Outline each uninfected red blood cell.
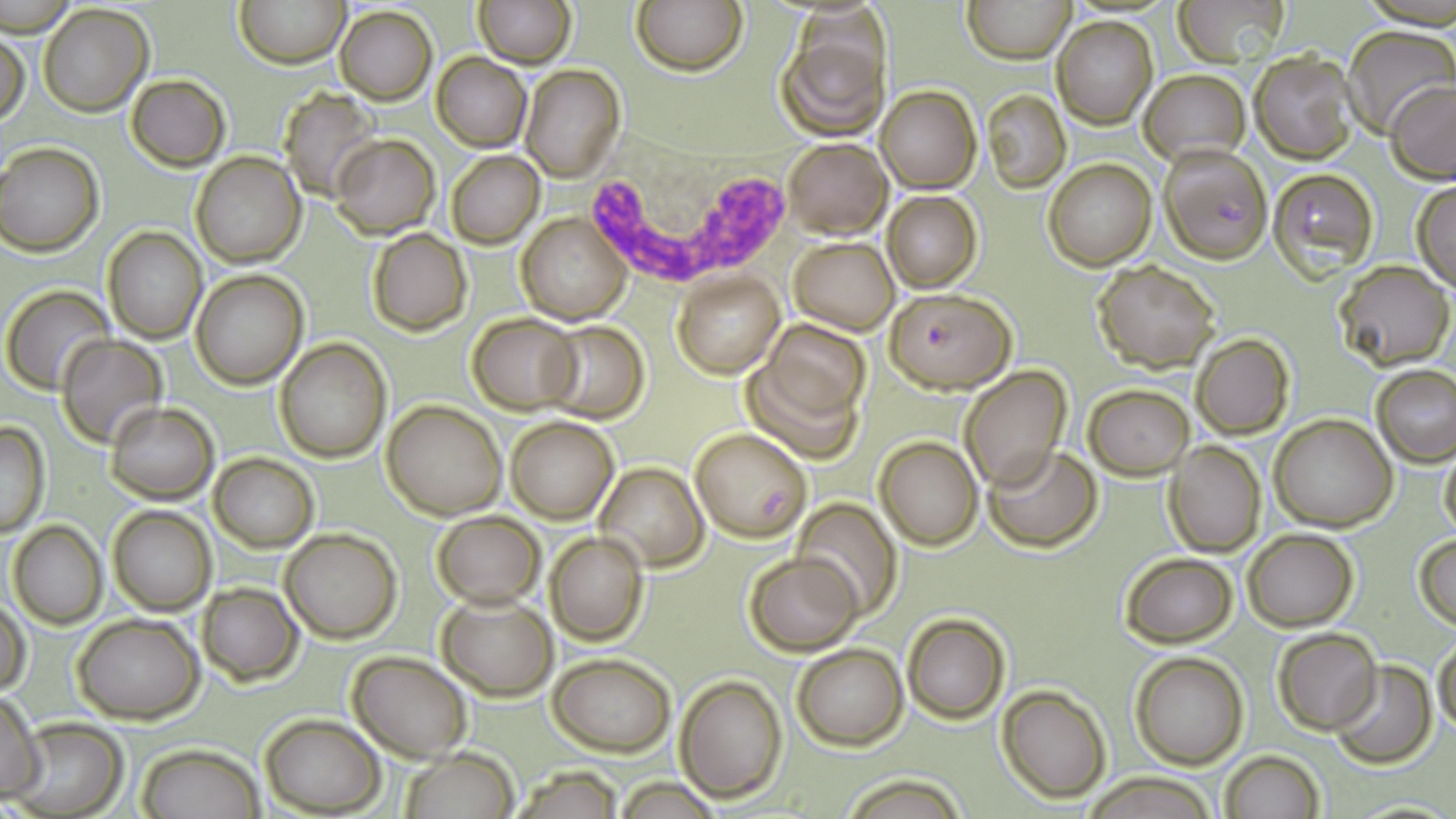
Approximate bounding boxes as named x1/y1/x2/y2 corners in pixels.
Uninfected red blood cells: (x1=236, y1=0, x2=348, y2=68), (x1=474, y1=0, x2=574, y2=68), (x1=633, y1=0, x2=745, y2=75), (x1=964, y1=0, x2=1073, y2=62), (x1=1175, y1=0, x2=1289, y2=66), (x1=39, y1=4, x2=154, y2=115), (x1=335, y1=6, x2=437, y2=104), (x1=1052, y1=16, x2=1157, y2=127), (x1=774, y1=19, x2=889, y2=143), (x1=1343, y1=26, x2=1454, y2=137), (x1=1, y1=28, x2=30, y2=129), (x1=1249, y1=50, x2=1359, y2=164), (x1=431, y1=53, x2=531, y2=151), (x1=519, y1=65, x2=626, y2=182), (x1=1138, y1=70, x2=1249, y2=167), (x1=127, y1=74, x2=230, y2=171), (x1=1385, y1=78, x2=1456, y2=183), (x1=876, y1=85, x2=981, y2=192), (x1=282, y1=86, x2=380, y2=200), (x1=984, y1=91, x2=1069, y2=191), (x1=332, y1=134, x2=439, y2=239), (x1=781, y1=138, x2=892, y2=238), (x1=0, y1=142, x2=104, y2=255), (x1=446, y1=149, x2=545, y2=248), (x1=190, y1=151, x2=306, y2=267), (x1=1044, y1=160, x2=1155, y2=270), (x1=1410, y1=182, x2=1456, y2=290), (x1=882, y1=191, x2=982, y2=293), (x1=517, y1=213, x2=630, y2=325), (x1=102, y1=228, x2=206, y2=344), (x1=367, y1=229, x2=471, y2=337), (x1=789, y1=237, x2=899, y2=334), (x1=1091, y1=259, x2=1221, y2=371), (x1=1331, y1=261, x2=1453, y2=369), (x1=190, y1=271, x2=307, y2=389), (x1=672, y1=272, x2=784, y2=379), (x1=2, y1=285, x2=114, y2=394), (x1=468, y1=313, x2=582, y2=414), (x1=539, y1=321, x2=649, y2=422), (x1=764, y1=322, x2=869, y2=422), (x1=1191, y1=333, x2=1294, y2=440), (x1=54, y1=334, x2=168, y2=446), (x1=275, y1=338, x2=390, y2=462), (x1=742, y1=355, x2=863, y2=466), (x1=1372, y1=365, x2=1456, y2=467), (x1=958, y1=366, x2=1070, y2=493), (x1=1082, y1=384, x2=1194, y2=479), (x1=381, y1=400, x2=507, y2=519), (x1=103, y1=401, x2=219, y2=503), (x1=1270, y1=414, x2=1397, y2=531), (x1=506, y1=416, x2=617, y2=524), (x1=0, y1=420, x2=50, y2=537), (x1=874, y1=436, x2=982, y2=550), (x1=1164, y1=441, x2=1265, y2=555), (x1=984, y1=444, x2=1102, y2=551), (x1=1438, y1=446, x2=1456, y2=541), (x1=208, y1=453, x2=318, y2=552), (x1=595, y1=462, x2=708, y2=571), (x1=791, y1=500, x2=904, y2=620), (x1=106, y1=504, x2=216, y2=616), (x1=431, y1=511, x2=544, y2=609), (x1=7, y1=521, x2=106, y2=628), (x1=281, y1=528, x2=401, y2=642), (x1=1242, y1=529, x2=1358, y2=631), (x1=545, y1=531, x2=648, y2=645), (x1=1413, y1=534, x2=1456, y2=629), (x1=1118, y1=551, x2=1238, y2=647), (x1=743, y1=552, x2=862, y2=656), (x1=196, y1=582, x2=304, y2=686), (x1=435, y1=591, x2=559, y2=701), (x1=1, y1=598, x2=31, y2=699), (x1=902, y1=613, x2=1009, y2=725), (x1=72, y1=614, x2=203, y2=723), (x1=1272, y1=628, x2=1382, y2=734), (x1=1433, y1=640, x2=1456, y2=736), (x1=790, y1=643, x2=907, y2=750), (x1=347, y1=650, x2=473, y2=762), (x1=1129, y1=650, x2=1250, y2=769), (x1=547, y1=651, x2=676, y2=755), (x1=1330, y1=660, x2=1436, y2=768), (x1=675, y1=673, x2=788, y2=802), (x1=996, y1=684, x2=1110, y2=803), (x1=0, y1=690, x2=46, y2=801), (x1=259, y1=714, x2=384, y2=815), (x1=9, y1=719, x2=129, y2=818), (x1=137, y1=743, x2=265, y2=819), (x1=398, y1=748, x2=519, y2=818), (x1=1218, y1=750, x2=1325, y2=818), (x1=839, y1=771, x2=970, y2=818), (x1=1087, y1=773, x2=1217, y2=817).

{
  "plasmodium_falciparum_infected_red_blood_cell_locations": "approximate bounding boxes as named x1/y1/x2/y2 corners in pixels: (x1=1160, y1=144, x2=1271, y2=263), (x1=1267, y1=168, x2=1379, y2=278), (x1=887, y1=288, x2=1016, y2=393), (x1=689, y1=428, x2=812, y2=541)",
  "slide_level_diagnosis": "Plasmodium falciparum",
  "white_blood_cell_locations": "approximate bounding boxes as named x1/y1/x2/y2 corners in pixels: (x1=578, y1=125, x2=823, y2=301)",
  "stain": "May-Grünwald-Giemsa",
  "field_of_view": "one of a larger specimen",
  "modality": "light microscopy",
  "magnification": "1000x",
  "preparation": "thin blood smear",
  "image_size": "1456×819 pixels"
}